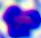
modality = photomicrograph
identification = leukocyte
magnification = 400x